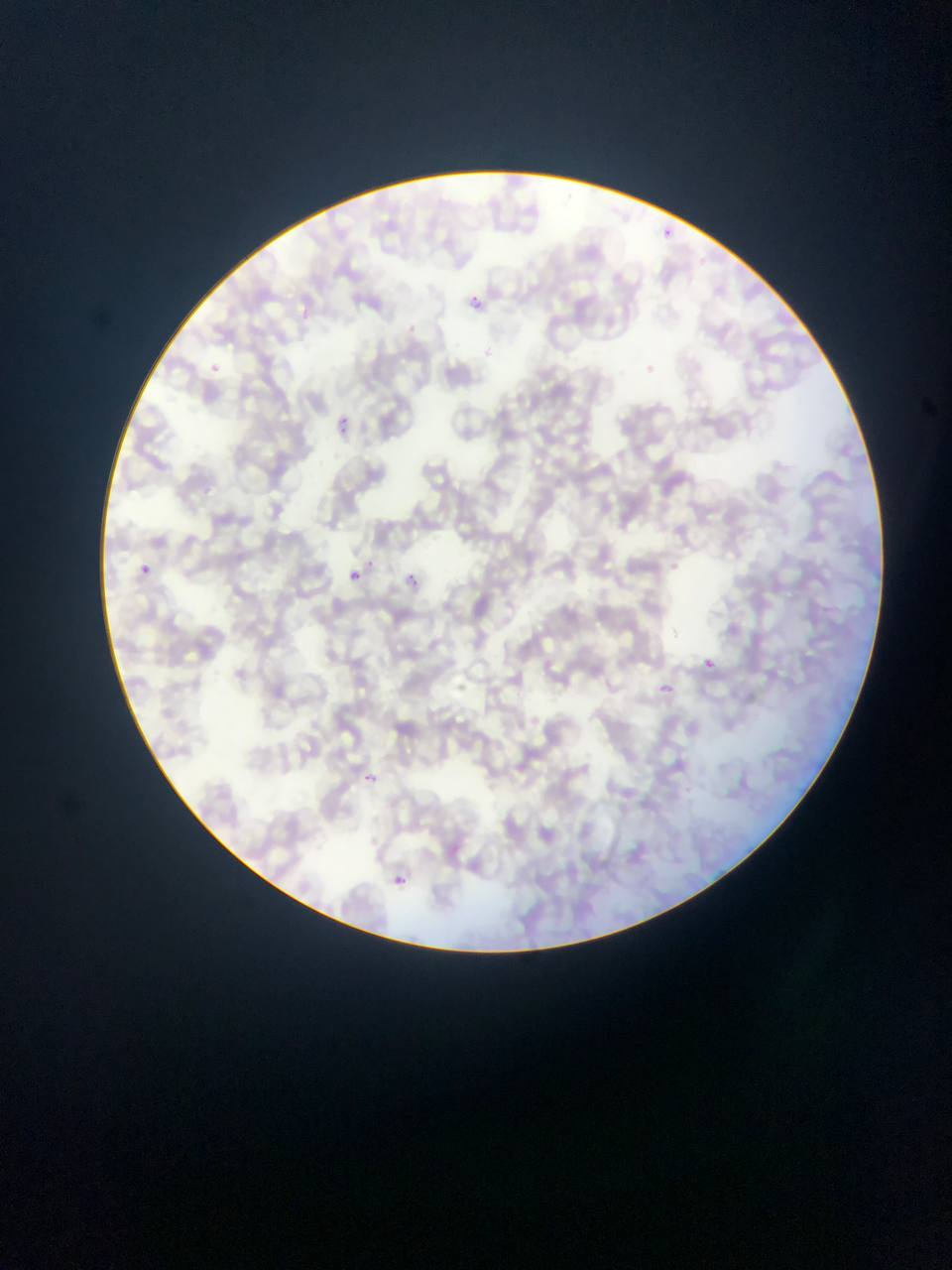

{
  "capture": "mobile-phone photograph through a microscope",
  "field_of_view": "single",
  "malaria_parasite_locations": "approximate bounding boxes as [left, top, right, bottom] in pixels: [660, 227, 674, 238], [467, 293, 486, 307], [403, 321, 437, 339], [207, 358, 224, 372], [337, 420, 347, 433], [140, 563, 152, 575], [406, 568, 428, 585], [349, 570, 360, 582], [704, 656, 719, 667], [366, 774, 375, 782], [395, 874, 410, 891]",
  "country": "Ghana",
  "preparation": "thin blood smear",
  "image_size": "952×1270 pixels"
}